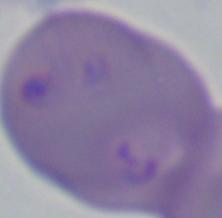
Summary:
  - Identification: Babesia
  - Magnification: 1000x
  - Modality: micrograph